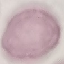
Summary:
  - Result: negative for malaria parasites
  - Preparation: thin smear
  - Stain: Giemsa
  - Capture: smartphone through the microscope eyepiece
  - Image type: automatically extracted cell patch, resized to 64 × 64 pixels